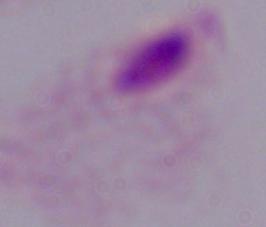

Summary:
  - Magnification: 1000x
  - Modality: micrograph
  - Identification: trichomonad